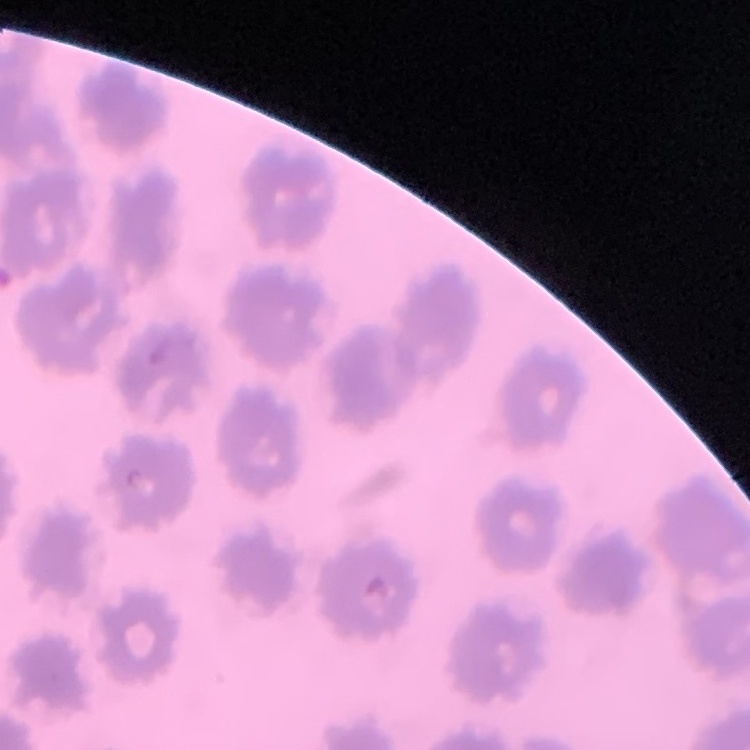
red blood cell morphology = no rouleaux formation
image type = one tile cut from a larger photomicrograph
preparation = thin blood film
stain = Field's or Giemsa